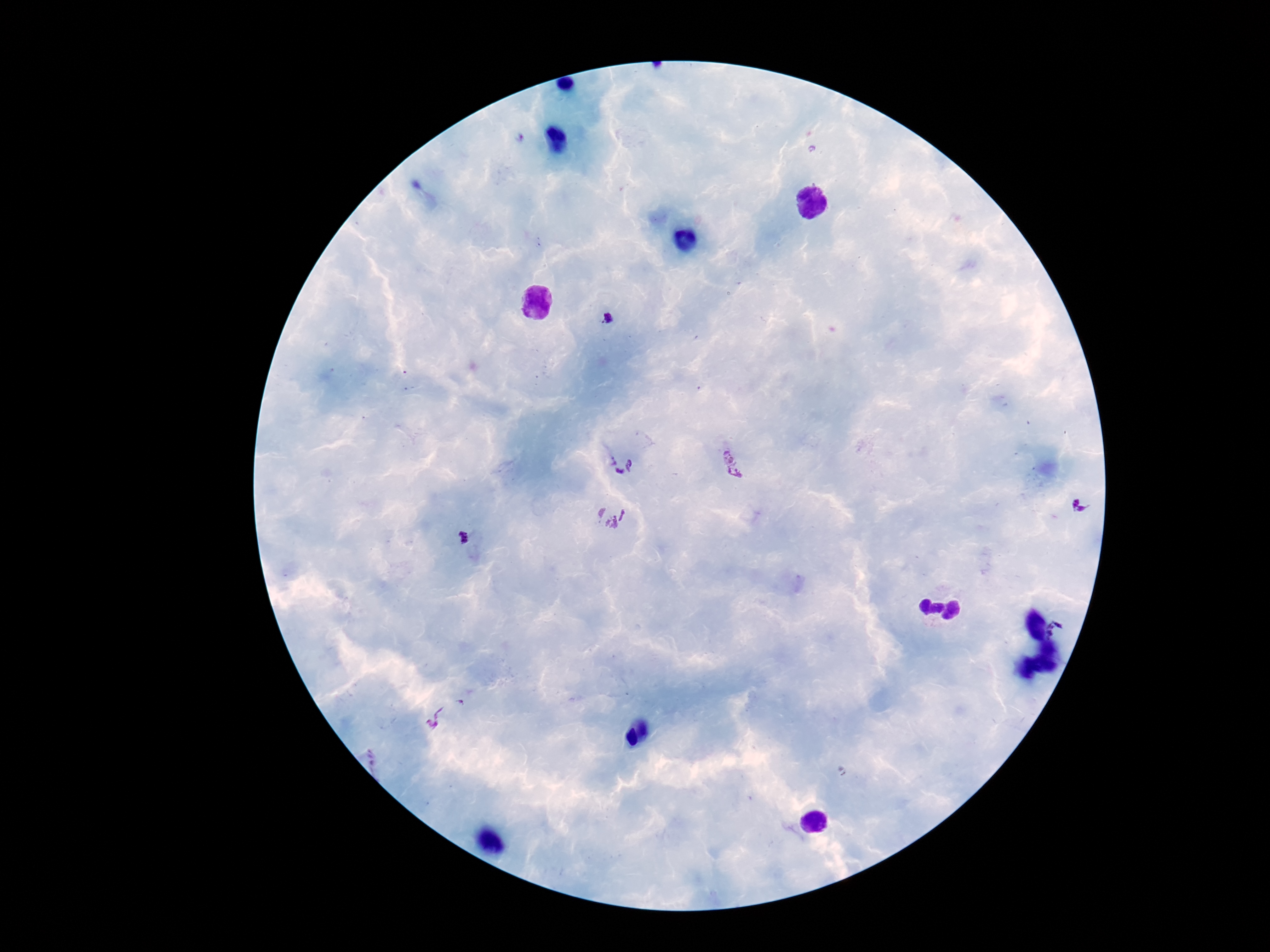
Approximate centers as {x, y} in pixels.
Summary:
  - Plasmodium parasite locations: {609, 318}, {621, 462}, {731, 463}, {1081, 503}, {611, 514}, {462, 537}, {1056, 631}, {444, 713}
  - Magnification: 100x
  - Capture: smartphone camera through the microscope eyepiece
  - Image size: 1270×952 pixels
  - Field of view: one from this slide
  - Preparation: thick blood smear
  - Patient malaria status: infected
  - Stain: Giemsa